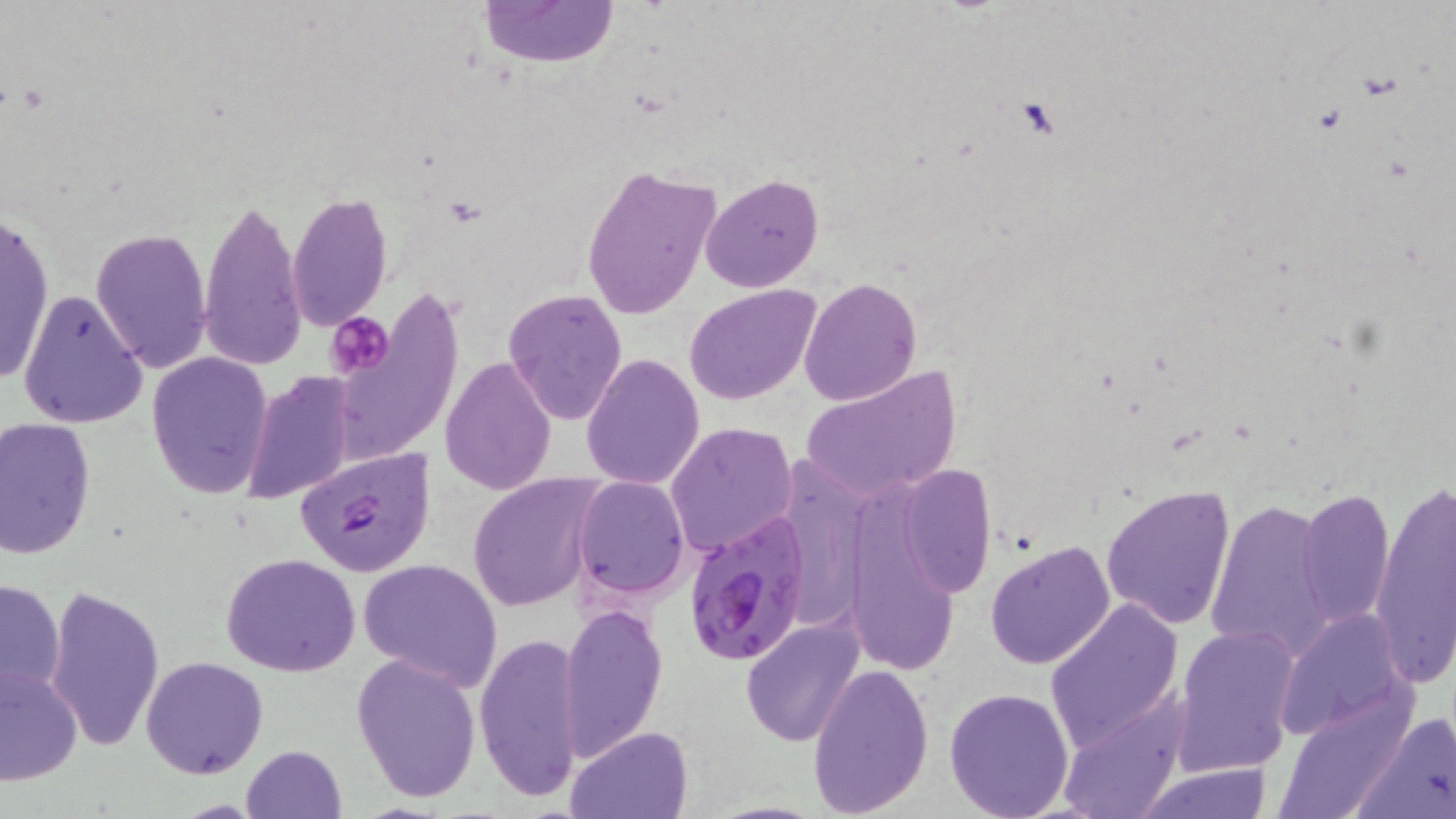

Summary:
  - Coordinate format: approximate bounding boxes as (x1, y1, x2, y2) in pixels
  - Platelet locations: (1015, 98, 1055, 137), (328, 312, 394, 379)
  - Uninfected red blood cell locations: (480, 0, 617, 67), (579, 163, 720, 320), (701, 172, 824, 293), (287, 191, 392, 330), (199, 194, 308, 373), (1, 206, 53, 390), (91, 226, 214, 371), (799, 277, 922, 407), (686, 284, 820, 404), (18, 288, 148, 430), (502, 288, 628, 425), (146, 352, 273, 499), (581, 353, 705, 490), (438, 356, 557, 495), (799, 367, 962, 501), (241, 372, 357, 505), (0, 417, 97, 559), (666, 422, 798, 559), (791, 453, 870, 639), (896, 463, 995, 597), (468, 472, 602, 611), (571, 475, 690, 598), (1369, 477, 1456, 687), (1101, 483, 1236, 629), (1297, 486, 1396, 630), (841, 489, 960, 672), (1205, 497, 1336, 660), (984, 539, 1116, 669), (221, 553, 363, 677), (358, 557, 503, 690), (0, 577, 67, 703), (43, 585, 164, 753), (1044, 599, 1185, 753), (558, 601, 666, 760), (1272, 610, 1411, 741), (741, 619, 865, 747), (1173, 626, 1299, 776), (473, 630, 584, 802), (350, 652, 482, 804), (141, 655, 269, 778), (0, 661, 83, 787), (807, 661, 935, 818), (943, 684, 1075, 818), (1053, 696, 1189, 819), (1271, 700, 1408, 818), (1360, 709, 1455, 817), (564, 724, 694, 817), (241, 744, 346, 819), (1134, 763, 1276, 819)
  - Plasmodium falciparum-infected red blood cell locations: (295, 445, 436, 577), (679, 512, 813, 665)
  - Slide-level diagnosis: Plasmodium falciparum
  - Stain: May-Grünwald-Giemsa
  - Magnification: 1000x
  - Image size: 1456×819 pixels
  - Preparation: thin blood smear
  - Field of view: single
  - Modality: optical microscopy